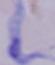 1000x magnification. Photomicrograph. A trypanosome is shown.